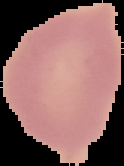 Result: no Plasmodium parasites detected. Image is 124×166 pixels. From a thin blood film. The area outside the segmented cell region is set to black.